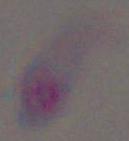 Micrograph. Toxoplasma gondii is shown. 1000x magnification.